Report the malaria status of this cell.
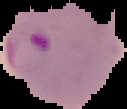
It is parasitized.

{
  "image_size": "127×109 pixels",
  "preparation": "thin blood film",
  "image_type": "segmented cell region on a black background"
}